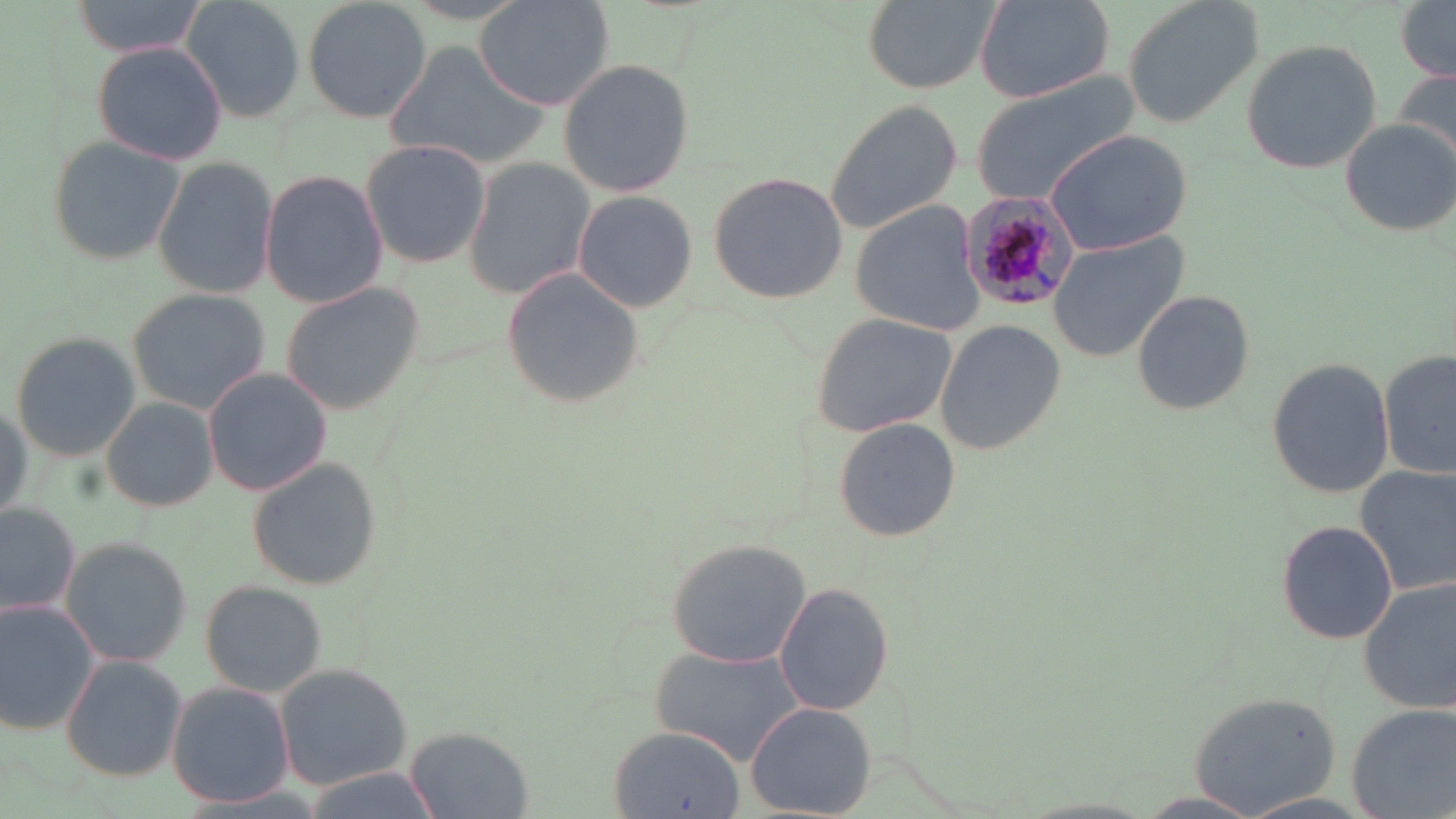

Approximate bounding boxes as (x1, y1, x2, y2) in pixels. Plasmodium malariae-infected red blood cell locations: (958, 189, 1079, 313). Uninfected red blood cell locations: (65, 0, 212, 58), (181, 0, 309, 122), (301, 0, 432, 124), (475, 0, 616, 110), (862, 0, 1003, 90), (1121, 0, 1265, 131), (976, 1, 1112, 102), (1396, 3, 1455, 81), (1240, 40, 1384, 176), (92, 42, 227, 165), (384, 42, 550, 169), (557, 58, 695, 197), (1391, 67, 1456, 174), (968, 74, 1142, 204), (824, 99, 962, 235), (1337, 118, 1456, 238), (1043, 127, 1191, 255), (47, 135, 189, 267), (360, 138, 490, 268), (152, 156, 278, 300), (463, 158, 595, 300), (258, 168, 389, 309), (708, 173, 845, 303), (573, 189, 700, 312), (848, 201, 990, 335), (1047, 232, 1189, 361), (501, 270, 650, 409), (278, 279, 429, 416), (125, 287, 270, 415), (1131, 289, 1254, 416), (808, 313, 959, 437), (935, 319, 1066, 452), (10, 332, 140, 461), (1381, 349, 1456, 483), (1266, 356, 1394, 501), (202, 367, 334, 498), (102, 398, 218, 511), (832, 418, 959, 543), (247, 460, 381, 591), (1355, 464, 1456, 595), (0, 500, 81, 620), (1278, 518, 1395, 644), (58, 535, 192, 667), (664, 536, 813, 668), (201, 580, 329, 696), (1360, 580, 1456, 713), (774, 581, 893, 715), (0, 599, 100, 734), (650, 645, 807, 766), (61, 654, 188, 782), (275, 663, 411, 790), (166, 683, 292, 808), (1188, 687, 1343, 817), (746, 702, 877, 817), (1349, 703, 1455, 818), (405, 725, 533, 818), (608, 726, 747, 818). Slide-level diagnosis: Plasmodium malariae. May-Grünwald-Giemsa-stained preparation. Thin blood smear. Single field of view. 1000x magnification. Image is 1456×819 pixels. Light microscopy.